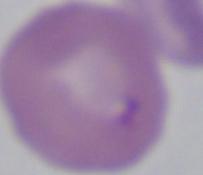

{
  "identification": "Babesia",
  "magnification": "1000x",
  "modality": "photomicrograph"
}